Point out each leukocyte.
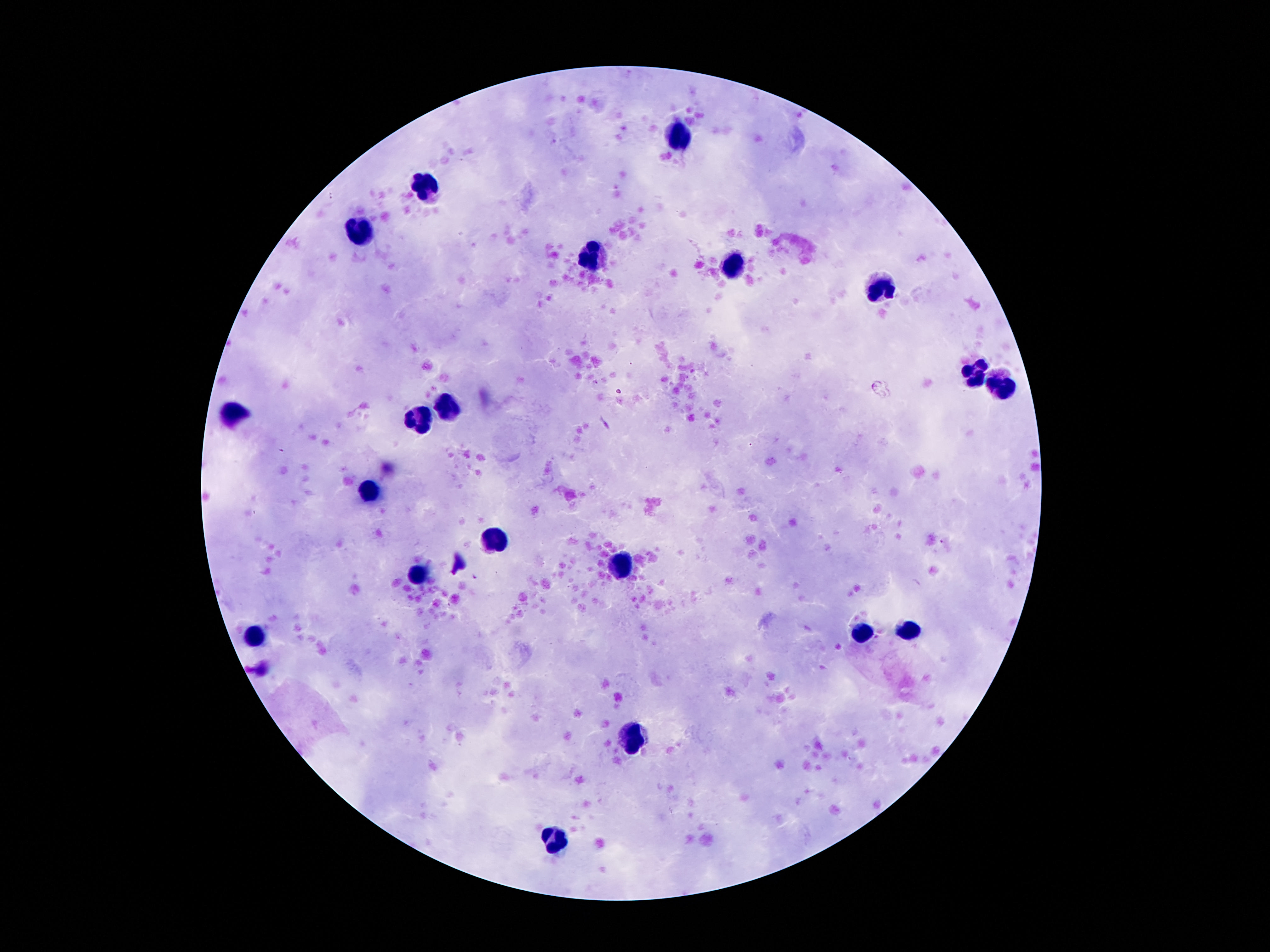

Approximate centers as {x, y} in pixels.
Leukocytes: {680, 139}, {422, 185}, {363, 233}, {596, 258}, {734, 270}, {882, 289}, {974, 377}, {1005, 387}, {449, 403}, {233, 414}, {421, 418}, {369, 490}, {495, 540}, {617, 563}, {422, 575}, {909, 628}, {862, 632}, {254, 636}, {634, 736}, {558, 840}.

Single field of view. Giemsa stain. Thick blood film. Smartphone photograph taken through the microscope eyepiece. Image is 1270×952 pixels. 100x magnification. Patient malaria status: not infected.